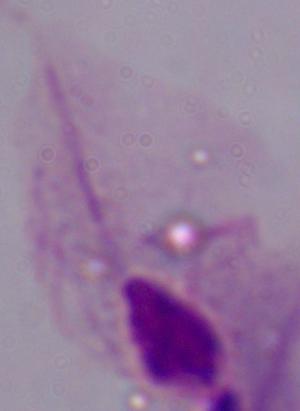
{
  "magnification": "1000x",
  "modality": "micrograph",
  "identification": "trichomonad"
}